Name the cell type shown.
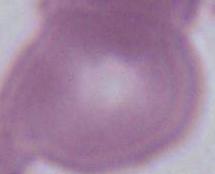

This is an erythrocyte.

Photomicrograph. Captured at 1000x magnification.